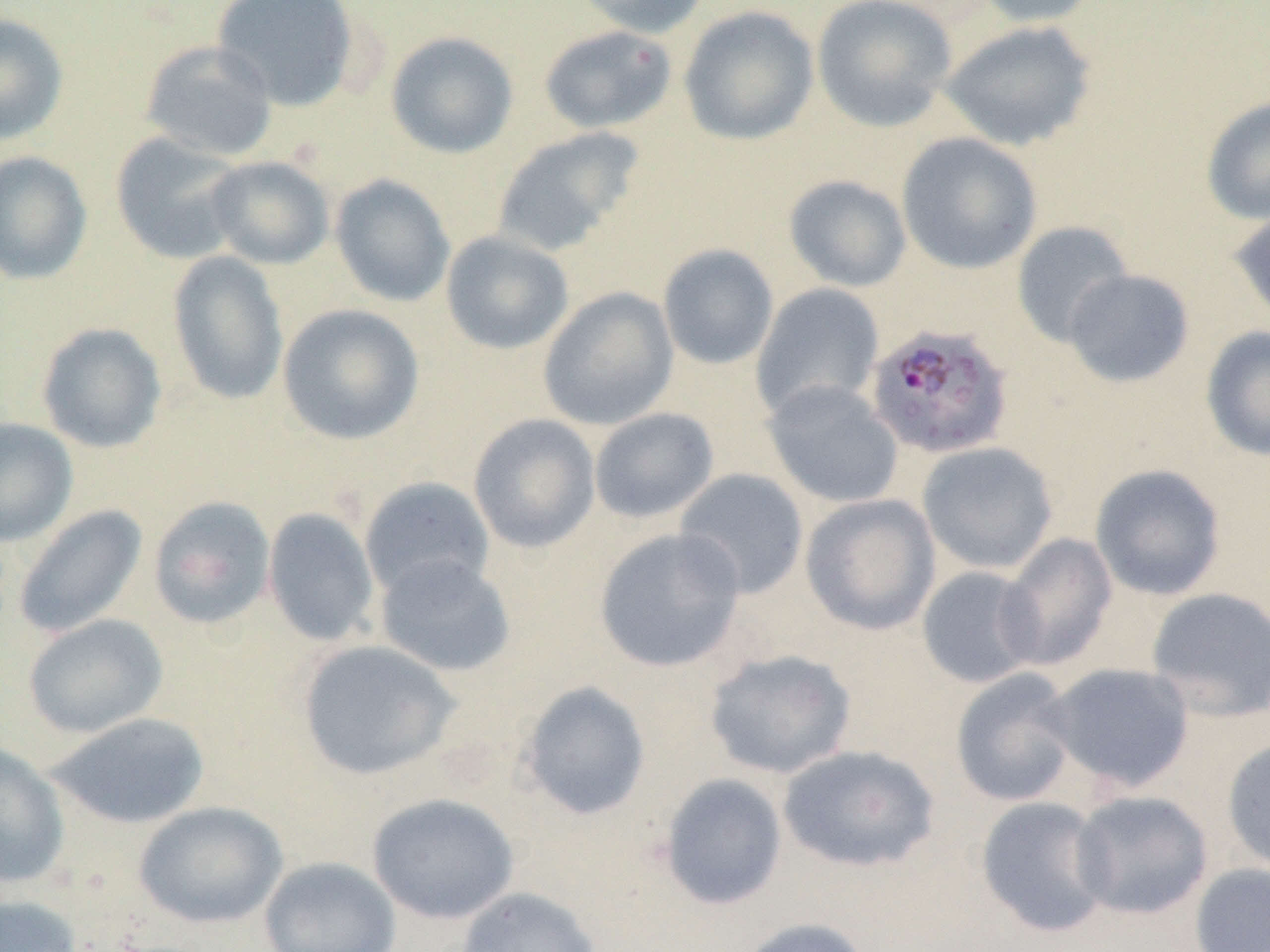

slide-level diagnosis = Plasmodium falciparum
image size = 1270×952 pixels
field of view = one of a larger specimen
modality = optical microscopy
Plasmodium falciparum-infected red blood cell locations = approximate bounding boxes as [x1, y1, x2, y2] in pixels: [867, 327, 1016, 463]
uninfected red blood cell locations = approximate bounding boxes as [x1, y1, x2, y2] in pixels: [211, 0, 359, 111], [570, 0, 713, 38], [811, 0, 958, 132], [970, 0, 1103, 27], [678, 5, 819, 145], [0, 12, 69, 145], [940, 19, 1097, 152], [539, 25, 677, 134], [385, 30, 519, 159], [139, 39, 279, 162], [1201, 96, 1270, 225], [491, 127, 643, 257], [896, 132, 1042, 274], [110, 133, 247, 265], [0, 151, 92, 285], [205, 155, 334, 269], [330, 174, 456, 307], [783, 175, 912, 292], [1230, 207, 1270, 327], [1011, 221, 1134, 347], [440, 231, 574, 355], [657, 243, 779, 370], [166, 251, 289, 406], [1062, 269, 1194, 388], [750, 283, 885, 419], [538, 287, 679, 431], [277, 303, 426, 446], [36, 322, 167, 453], [1201, 325, 1270, 461], [762, 379, 904, 509], [589, 407, 720, 524], [467, 413, 601, 553], [0, 417, 79, 546], [916, 441, 1059, 574], [1090, 463, 1227, 601], [673, 468, 809, 599], [359, 477, 495, 600], [799, 493, 942, 635], [148, 495, 276, 630], [12, 505, 148, 639], [262, 508, 379, 646], [593, 526, 747, 673], [997, 533, 1118, 671], [373, 553, 517, 677], [916, 565, 1043, 689], [1145, 587, 1270, 722], [23, 614, 169, 738], [296, 640, 461, 780], [703, 648, 858, 779], [1043, 662, 1195, 793], [949, 668, 1081, 808], [518, 680, 651, 820], [45, 711, 211, 829], [1221, 737, 1270, 876], [0, 743, 70, 888], [777, 744, 940, 873], [658, 773, 788, 910], [1070, 790, 1213, 920], [368, 793, 519, 924], [973, 796, 1114, 938], [134, 801, 287, 929], [259, 856, 401, 952], [1189, 863, 1270, 952], [456, 886, 603, 951], [0, 894, 83, 952], [737, 917, 873, 952]
preparation = thin blood smear
magnification = 1000x